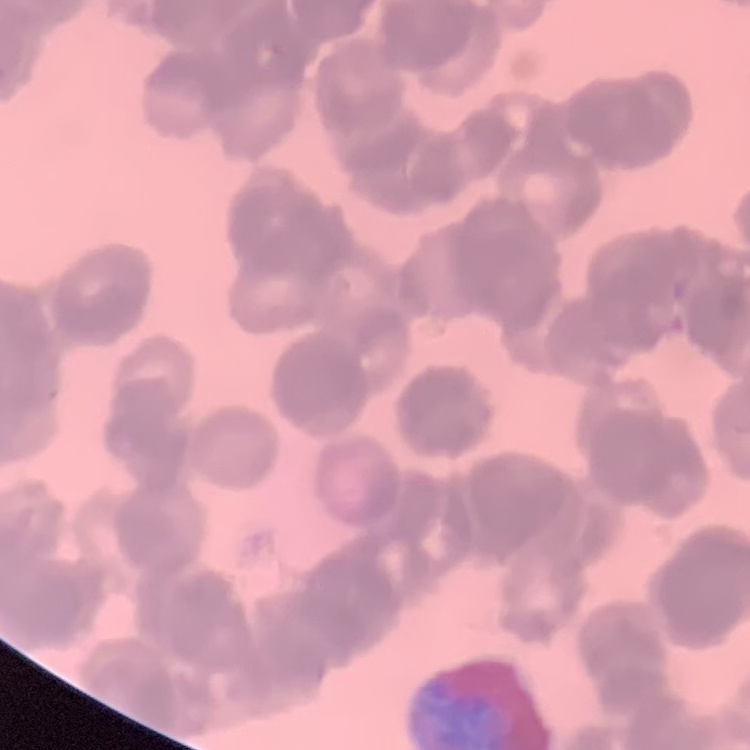
Summary:
  - Erythrocyte morphology: rouleaux formation
  - Preparation: thin peripheral smear
  - Image type: one tile cut from a larger photomicrograph
  - Stain: Field's or Giemsa